Report the malaria status of this cell.
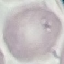
Uninfected.

{
  "stain": "Giemsa",
  "capture": "smartphone camera at the microscope eyepiece",
  "image_type": "automatically extracted cell patch, resized to 64 × 64 pixels",
  "preparation": "thin smear"
}